Report the malaria status of this cell.
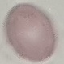

Uninfected.

Summary:
  - Stain: Giemsa
  - Image type: cell patch, automatically extracted from a larger field of view and resized to 64 × 64 pixels
  - Capture: smartphone camera at the microscope eyepiece
  - Preparation: thin blood smear